Point out each Plasmodium parasite and each leukocyte.
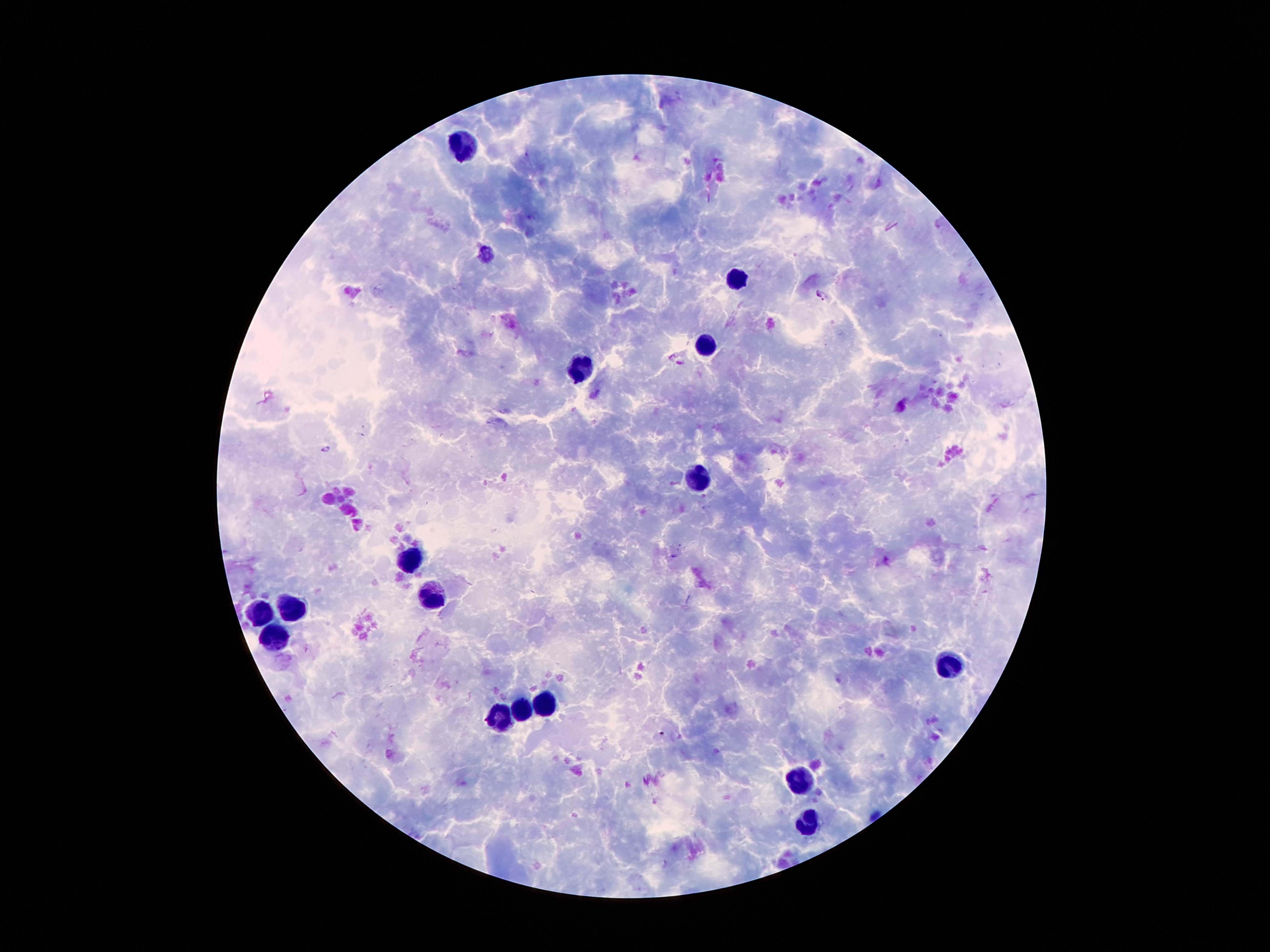

Approximate centers as {x, y} in pixels.
Plasmodium parasites: {822, 295}, {328, 449}.
Leukocytes: {465, 143}, {740, 279}, {703, 347}, {576, 368}, {699, 479}, {412, 557}, {428, 597}, {290, 609}, {260, 614}, {274, 638}, {948, 664}, {546, 706}, {521, 711}, {499, 722}, {799, 781}, {808, 823}.

field of view = single
magnification = 100x
stain = Giemsa
patient malaria status = positive for Plasmodium falciparum
capture = smartphone camera through the microscope eyepiece
image size = 1270×952 pixels
preparation = thick blood film